Assess this cell for malaria.
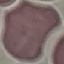
Uninfected.

Acquired by smartphone through the microscope eyepiece. Giemsa stain. Automatically extracted cell patch, resized to 64 × 64 pixels. Thin blood smear.